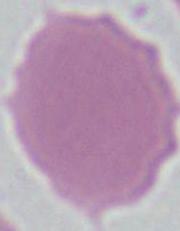

An erythrocyte is shown. Micrograph. Captured at 1000x magnification.